Classify this cell by malaria status.
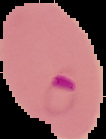

Parasitized.

Summary:
  - Preparation: thin blood film
  - Image size: 106×139 pixels
  - Image type: segmented cell region with the area outside set to black